Report the malaria status of this cell.
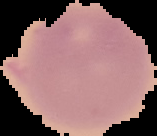

It is uninfected.

image type = segmented cell region with the area outside set to black
preparation = thin blood smear
image size = 157×136 pixels